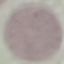
malaria status = uninfected
preparation = thin smear
stain = Giemsa
image type = cell patch, automatically extracted from a larger field of view and resized to 64 × 64 pixels
capture = smartphone through the microscope eyepiece